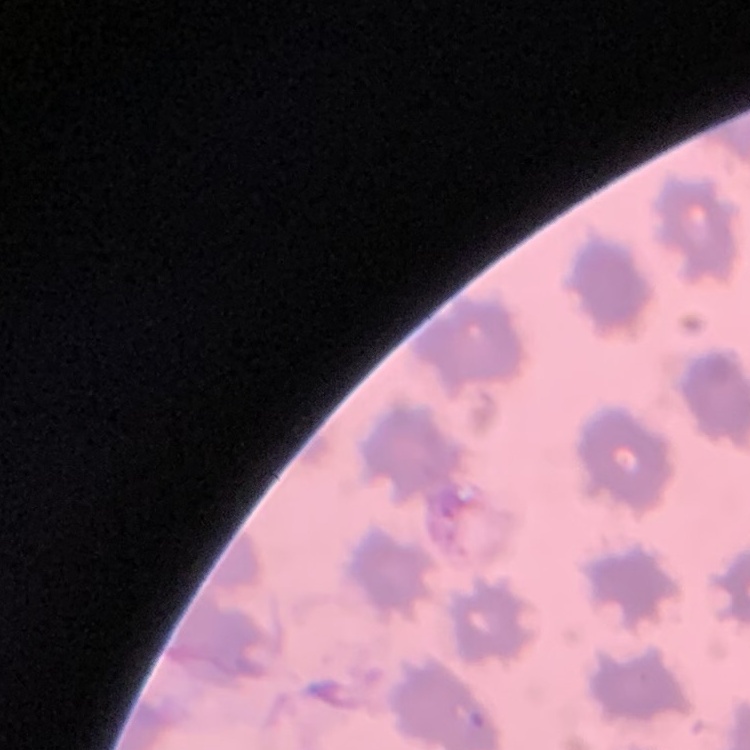
The red blood cells exhibit no rouleaux formation. Stained with either Field's or Giemsa. Square crop of a larger photomicrograph. Thin blood film.